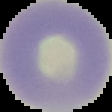

malaria_status: uninfected
preparation: thin blood film
image_type: cell region segmented out of the field of view; surrounding area masked to black
image_size: 112×112 pixels